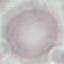
Summary:
  - Malaria status: uninfected
  - Stain: Giemsa
  - Capture: smartphone through the microscope eyepiece
  - Image type: cell patch, automatically extracted from a larger field of view and resized to 64 × 64 pixels
  - Preparation: thin blood smear